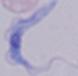

{
  "modality": "photomicrograph",
  "magnification": "1000x",
  "identification": "trypanosome"
}